Name the parasite shown.
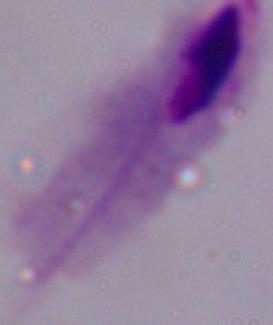

This is a trichomonad.

modality = photomicrograph
magnification = 1000x